State which parasite is depicted.
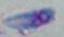

Toxoplasma gondii.

Photomicrograph. 1000x magnification.